Outline each uninfected red blood cell.
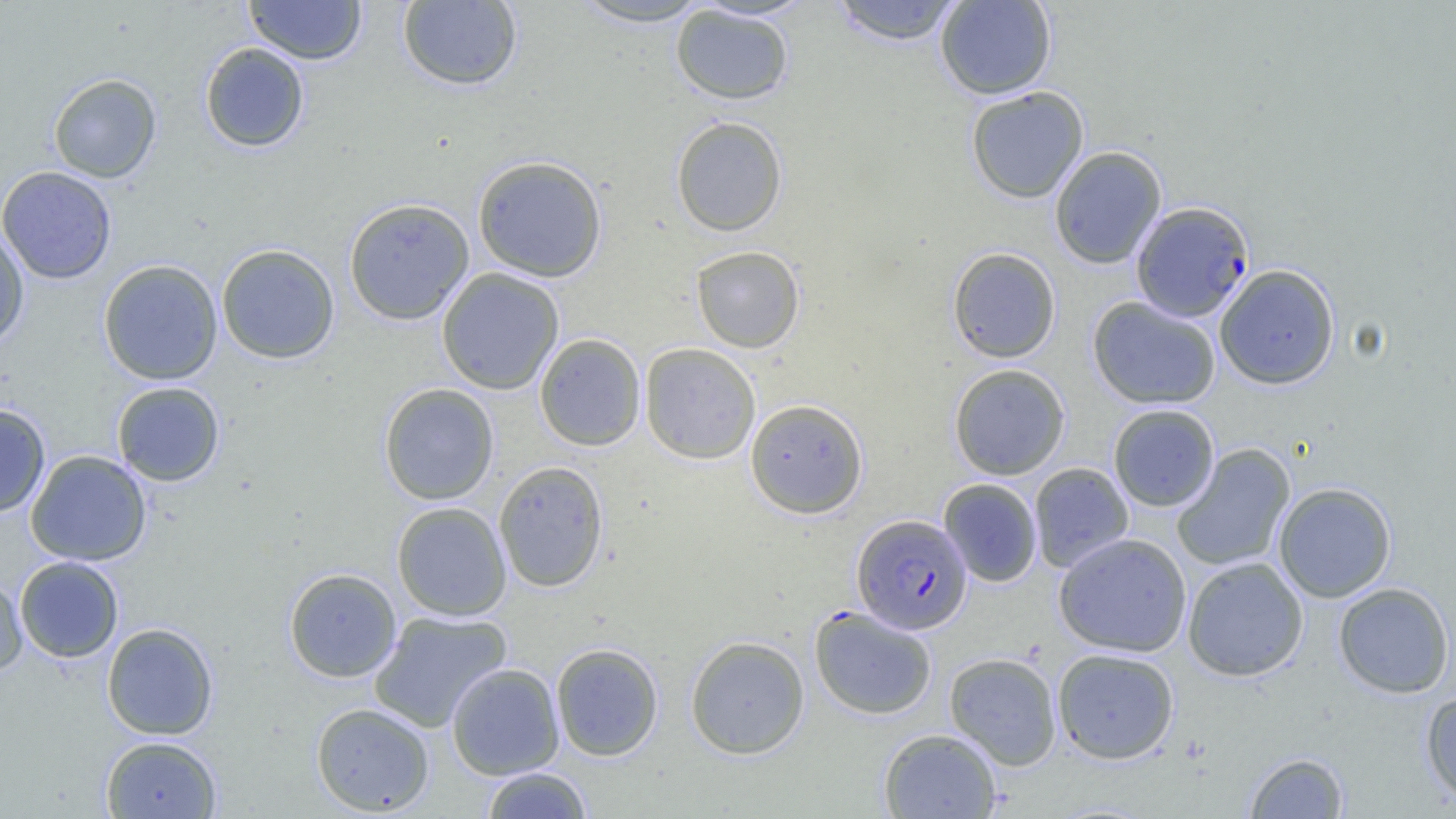

Approximate bounding boxes as named x1/y1/x2/y2 corners in pixels.
Uninfected red blood cells: (x1=245, y1=0, x2=366, y2=65), (x1=569, y1=0, x2=714, y2=27), (x1=934, y1=0, x2=1057, y2=99), (x1=397, y1=1, x2=523, y2=91), (x1=829, y1=1, x2=964, y2=46), (x1=671, y1=4, x2=794, y2=105), (x1=199, y1=42, x2=310, y2=153), (x1=48, y1=73, x2=162, y2=183), (x1=965, y1=86, x2=1089, y2=203), (x1=671, y1=116, x2=788, y2=237), (x1=1049, y1=146, x2=1167, y2=269), (x1=472, y1=154, x2=608, y2=283), (x1=0, y1=166, x2=117, y2=284), (x1=343, y1=197, x2=475, y2=326), (x1=0, y1=224, x2=29, y2=350), (x1=215, y1=243, x2=340, y2=364), (x1=691, y1=245, x2=805, y2=353), (x1=947, y1=247, x2=1060, y2=363), (x1=98, y1=259, x2=223, y2=385), (x1=1215, y1=264, x2=1340, y2=389), (x1=436, y1=268, x2=564, y2=395), (x1=1087, y1=297, x2=1221, y2=409), (x1=534, y1=333, x2=646, y2=451), (x1=640, y1=342, x2=760, y2=464), (x1=949, y1=363, x2=1070, y2=480), (x1=111, y1=381, x2=225, y2=487), (x1=378, y1=383, x2=499, y2=505), (x1=745, y1=398, x2=868, y2=519), (x1=0, y1=403, x2=51, y2=516), (x1=1108, y1=403, x2=1219, y2=512), (x1=1171, y1=444, x2=1296, y2=571), (x1=26, y1=450, x2=152, y2=566), (x1=493, y1=461, x2=609, y2=592), (x1=1029, y1=462, x2=1134, y2=573), (x1=938, y1=478, x2=1042, y2=587), (x1=1273, y1=482, x2=1396, y2=602), (x1=392, y1=502, x2=511, y2=621), (x1=1053, y1=532, x2=1192, y2=657), (x1=14, y1=556, x2=124, y2=663), (x1=1182, y1=557, x2=1309, y2=681), (x1=284, y1=568, x2=402, y2=682), (x1=0, y1=574, x2=27, y2=677), (x1=1333, y1=582, x2=1455, y2=698), (x1=810, y1=605, x2=937, y2=719), (x1=369, y1=610, x2=512, y2=733), (x1=102, y1=622, x2=219, y2=740), (x1=685, y1=635, x2=810, y2=759), (x1=550, y1=642, x2=664, y2=761), (x1=1051, y1=648, x2=1179, y2=764), (x1=944, y1=652, x2=1062, y2=770), (x1=446, y1=662, x2=564, y2=779), (x1=1421, y1=690, x2=1456, y2=807), (x1=310, y1=702, x2=435, y2=815), (x1=878, y1=728, x2=1001, y2=818), (x1=100, y1=736, x2=222, y2=818), (x1=1244, y1=752, x2=1349, y2=818), (x1=481, y1=767, x2=593, y2=818).

Plasmodium falciparum-infected red blood cell locations: (x1=1131, y1=201, x2=1254, y2=322), (x1=851, y1=514, x2=972, y2=635). Slide-level diagnosis: Plasmodium falciparum. Thin blood smear. One field of a larger specimen. Image is 1456×819 pixels. Captured at 1000x magnification. Optical microscopy.